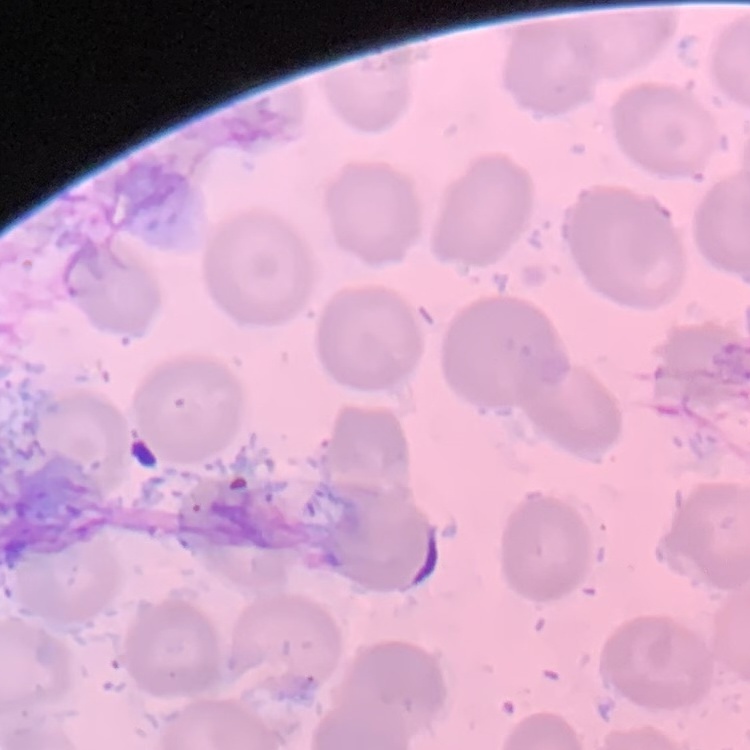

The red blood cells exhibit no rouleaux formation. Square crop of a larger photomicrograph. Thin peripheral smear. Stained with either Field's or Giemsa.